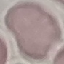

Summary:
  - Malaria status: uninfected
  - Capture: smartphone camera at the microscope eyepiece
  - Preparation: thin blood film
  - Image type: cell patch, automatically extracted from a larger field of view and resized to 64 × 64 pixels
  - Stain: Giemsa